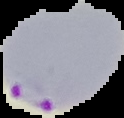
Segmented cell region on a black background. Result: malaria parasites identified. Image is 124×118 pixels. From a thin blood smear.